Locate every Plasmodium ovale-infected red blood cell.
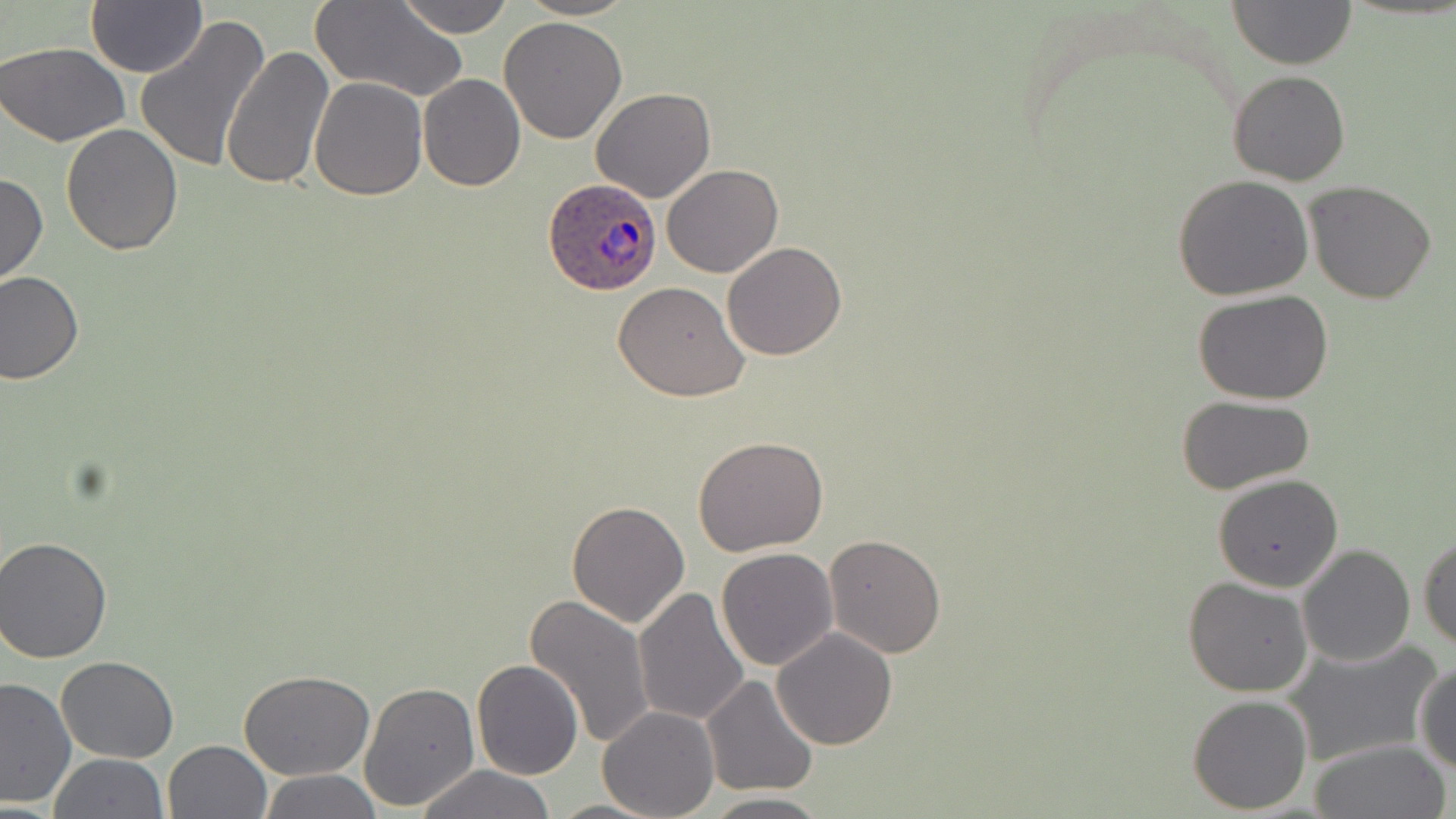
Approximate bounding boxes as named x1/y1/x2/y2 corners in pixels.
Plasmodium ovale-infected red blood cells: (x1=543, y1=178, x2=663, y2=295).

Summary:
  - Uninfected red blood cell locations: (x1=397, y1=0, x2=514, y2=38), (x1=517, y1=0, x2=637, y2=21), (x1=1229, y1=0, x2=1356, y2=69), (x1=85, y1=1, x2=207, y2=77), (x1=313, y1=1, x2=466, y2=103), (x1=133, y1=13, x2=271, y2=174), (x1=498, y1=17, x2=627, y2=143), (x1=0, y1=40, x2=131, y2=147), (x1=223, y1=44, x2=333, y2=189), (x1=1228, y1=70, x2=1349, y2=186), (x1=418, y1=74, x2=525, y2=191), (x1=310, y1=78, x2=427, y2=200), (x1=590, y1=89, x2=715, y2=204), (x1=59, y1=122, x2=184, y2=255), (x1=662, y1=164, x2=783, y2=278), (x1=0, y1=173, x2=48, y2=286), (x1=1173, y1=176, x2=1315, y2=299), (x1=1304, y1=180, x2=1436, y2=303), (x1=722, y1=241, x2=847, y2=360), (x1=0, y1=271, x2=83, y2=385), (x1=612, y1=281, x2=749, y2=403), (x1=1192, y1=291, x2=1335, y2=405), (x1=1175, y1=395, x2=1317, y2=492), (x1=693, y1=436, x2=829, y2=557), (x1=1213, y1=472, x2=1343, y2=592), (x1=566, y1=499, x2=691, y2=628), (x1=823, y1=534, x2=947, y2=658), (x1=1418, y1=534, x2=1456, y2=653), (x1=2, y1=535, x2=116, y2=662), (x1=1297, y1=543, x2=1416, y2=666), (x1=716, y1=548, x2=838, y2=670), (x1=1183, y1=577, x2=1313, y2=697), (x1=634, y1=585, x2=750, y2=727), (x1=525, y1=592, x2=654, y2=751), (x1=771, y1=627, x2=897, y2=750), (x1=1281, y1=638, x2=1443, y2=769), (x1=56, y1=656, x2=179, y2=763), (x1=472, y1=659, x2=584, y2=780), (x1=1414, y1=661, x2=1456, y2=774), (x1=240, y1=671, x2=372, y2=780), (x1=701, y1=674, x2=819, y2=797), (x1=0, y1=675, x2=74, y2=808), (x1=359, y1=681, x2=480, y2=813), (x1=1187, y1=694, x2=1312, y2=812), (x1=598, y1=706, x2=719, y2=819), (x1=1308, y1=739, x2=1453, y2=819), (x1=161, y1=740, x2=271, y2=819), (x1=50, y1=753, x2=167, y2=818), (x1=415, y1=765, x2=557, y2=819), (x1=255, y1=770, x2=383, y2=819), (x1=698, y1=792, x2=830, y2=818), (x1=548, y1=798, x2=660, y2=818)
  - Slide-level diagnosis: Plasmodium ovale
  - Image size: 1456×819 pixels
  - Field of view: single
  - Preparation: thin blood film
  - Modality: light microscopy
  - Magnification: 1000x
  - Stain: May-Grünwald-Giemsa